Classify this cell by malaria status.
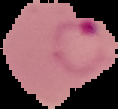
It is parasitized.

Summary:
  - Preparation: thin blood film
  - Image size: 118×109 pixels
  - Image type: cell region segmented out of the field of view; surrounding area masked to black